Comment on the morphology of the erythrocytes.
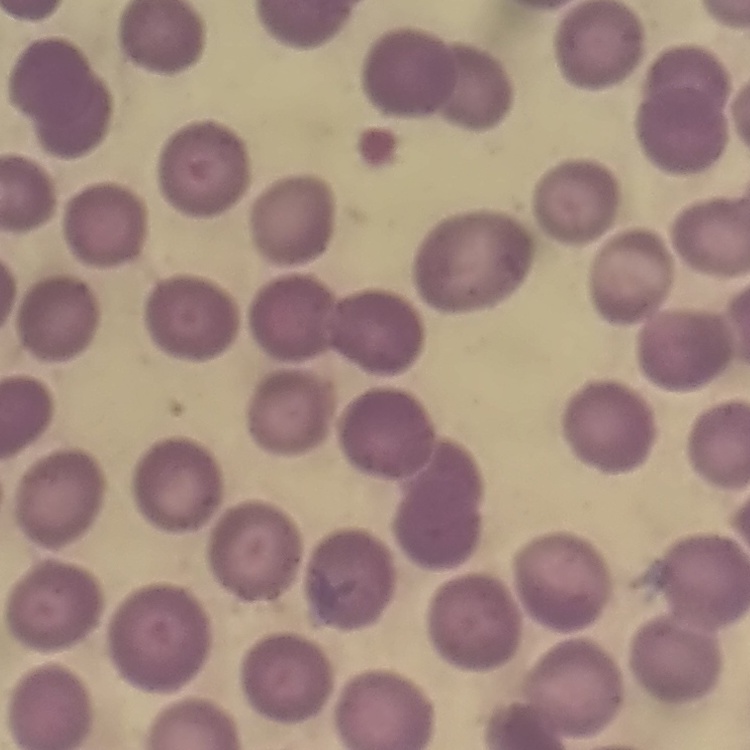
No rouleaux formation.

{
  "image_type": "one tile cut from a larger photomicrograph",
  "preparation": "thin blood smear",
  "stain": "Field's or Giemsa"
}